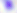
magnification = 400x
modality = micrograph
identification = Toxoplasma gondii